Point out each Plasmodium parasite.
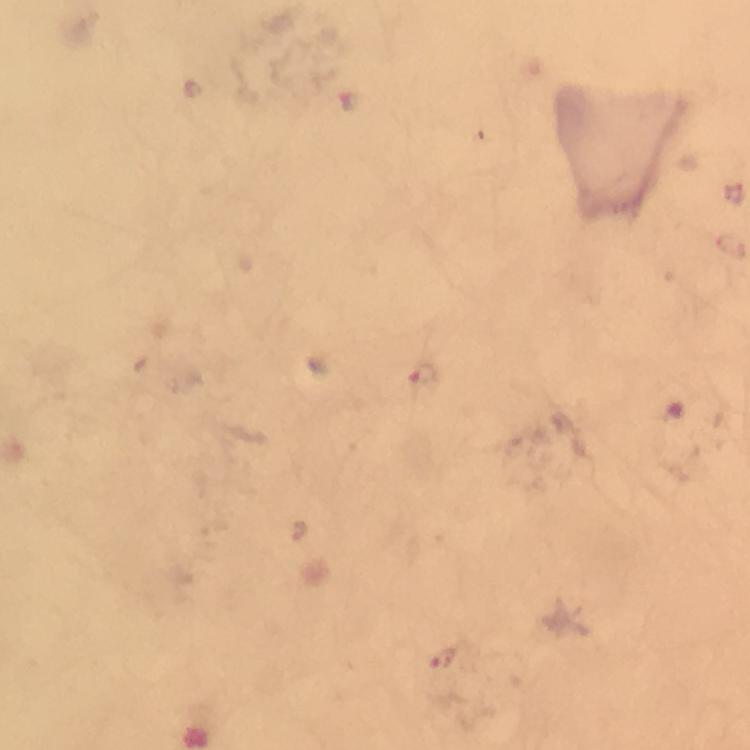
Approximate object centers, in pixels from the top-left corner.
Plasmodium parasites: (x=423, y=378), (x=442, y=660).

Summary:
  - Context: from a malaria diagnostic workup
  - Preparation: thick blood film
  - Capture: smartphone camera through the microscope
  - Stain: Giemsa
  - Magnification: 100x
  - Image size: 750×750 pixels
  - Immersion oil: used
  - Cropped from: a single field of view